Name the parasite shown.
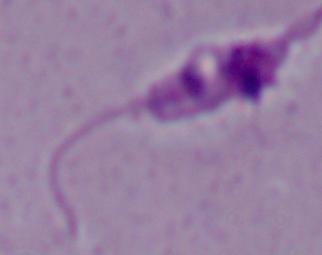
Leishmania.

Summary:
  - Modality: micrograph
  - Magnification: 1000x